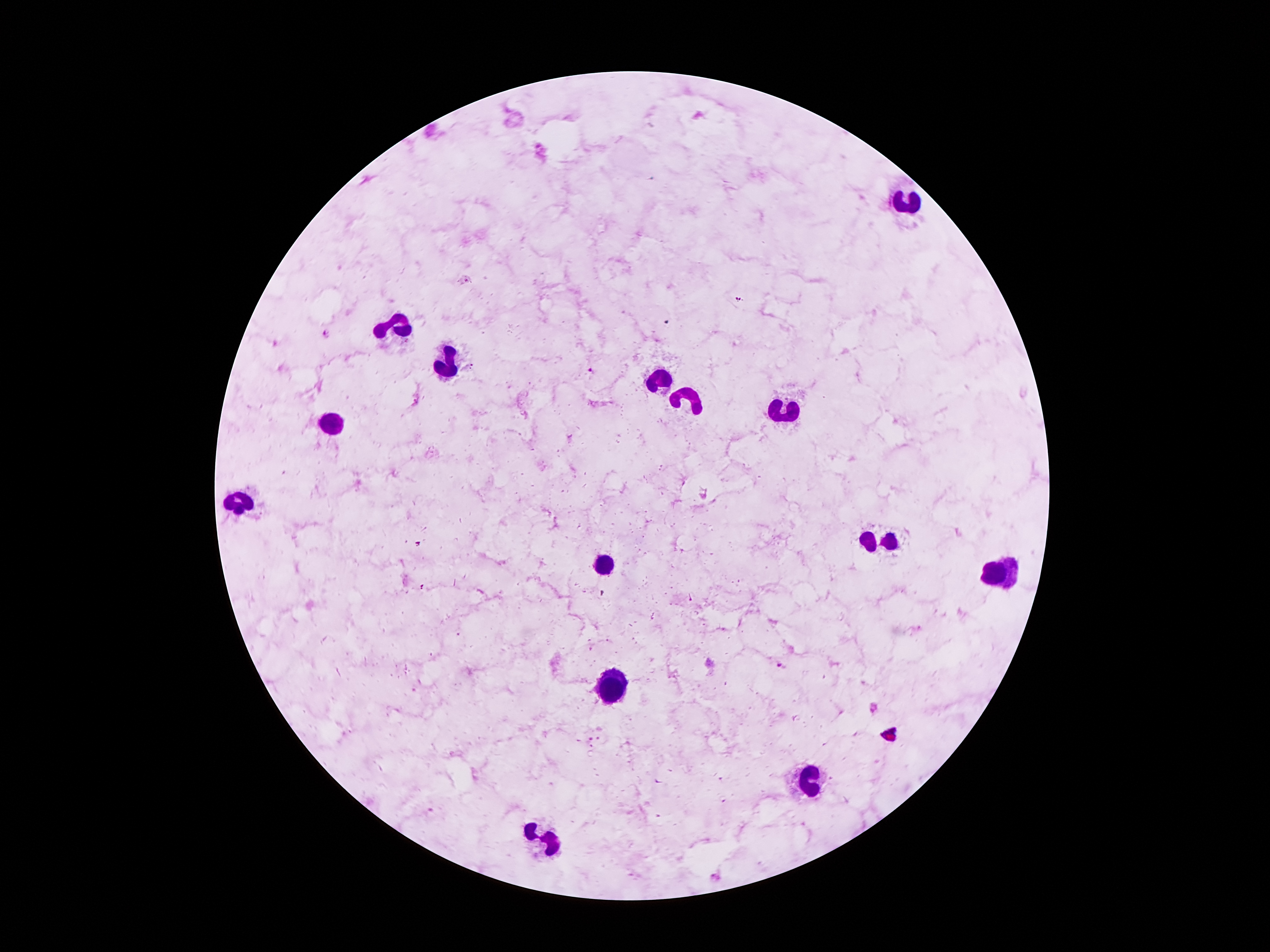
coordinate format = approximate centers as {x, y} in pixels
leukocyte locations = {909, 202}, {394, 325}, {445, 366}, {663, 379}, {689, 399}, {784, 407}, {333, 424}, {236, 508}, {876, 539}, {605, 564}, {1001, 573}, {611, 681}, {807, 782}, {547, 842}
Plasmodium parasite locations = {465, 279}, {738, 298}, {326, 333}, {472, 365}, {589, 370}, {782, 664}, {875, 707}, {589, 737}, {598, 738}, {716, 878}
preparation = thick peripheral-blood smear
field of view = one from this slide
magnification = 100x
image size = 1270×952 pixels
stain = Giemsa
capture = smartphone through the microscope eyepiece
patient malaria status = infected with Plasmodium falciparum